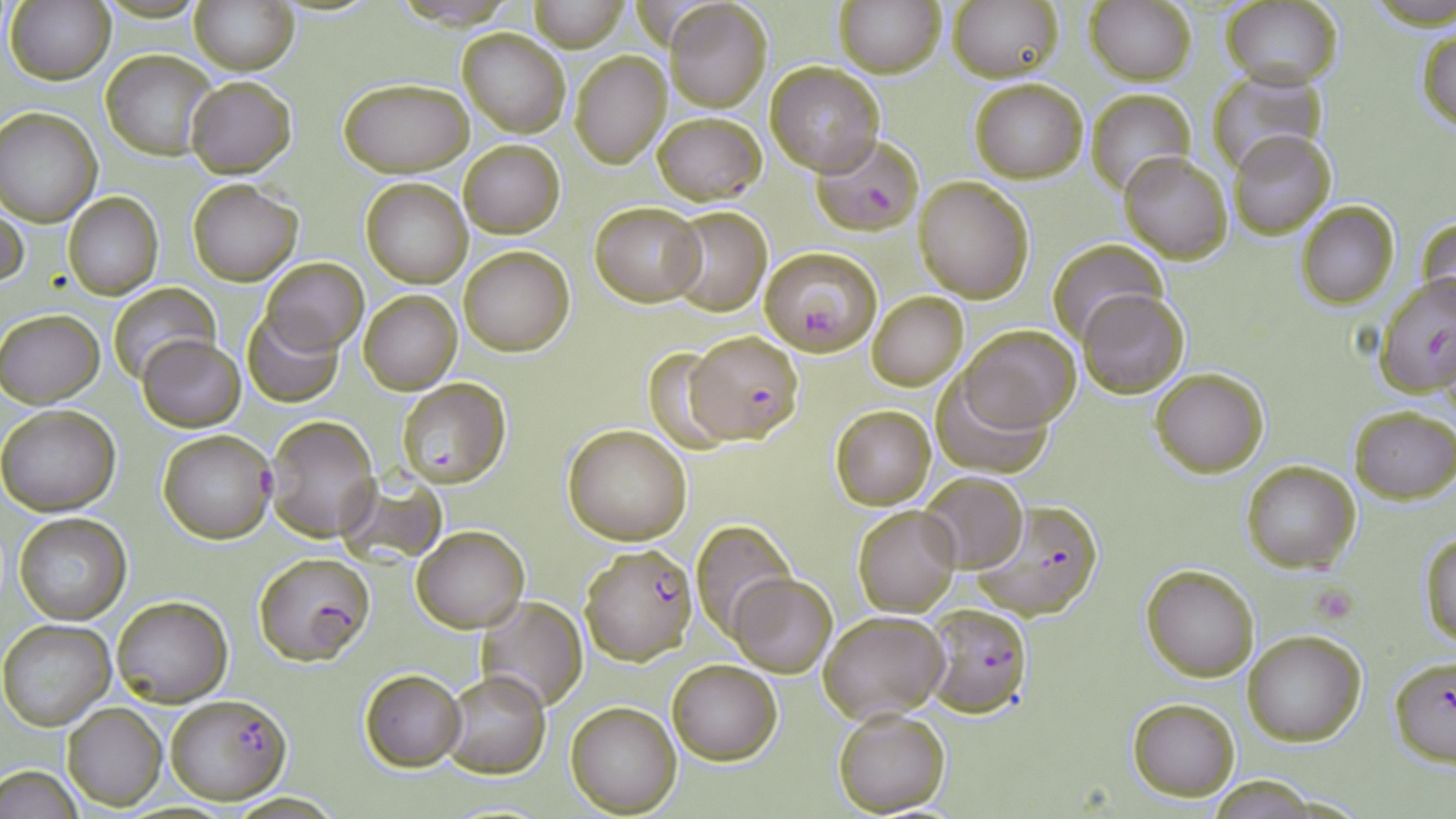

{
  "slide_level_diagnosis": "Plasmodium falciparum",
  "image_size": "1456×819 pixels",
  "magnification": "1000x",
  "preparation": "thin blood film",
  "modality": "optical microscopy",
  "stain": "May-Grünwald-Giemsa",
  "uninfected_red_blood_cell_locations_subset": "approximate bounding boxes as named x1/y1/x2/y2 corners in pixels: (x1=189, y1=0, x2=301, y2=74), (x1=529, y1=0, x2=628, y2=51), (x1=834, y1=0, x2=945, y2=77), (x1=664, y1=1, x2=772, y2=112), (x1=6, y1=2, x2=114, y2=84), (x1=948, y1=2, x2=1064, y2=81), (x1=1085, y1=2, x2=1195, y2=85), (x1=1221, y1=2, x2=1343, y2=89), (x1=1416, y1=28, x2=1456, y2=134), (x1=459, y1=29, x2=570, y2=137), (x1=100, y1=49, x2=215, y2=159), (x1=570, y1=49, x2=672, y2=168), (x1=766, y1=62, x2=886, y2=177), (x1=1206, y1=69, x2=1326, y2=177), (x1=185, y1=76, x2=296, y2=177), (x1=968, y1=76, x2=1088, y2=184), (x1=337, y1=77, x2=474, y2=176), (x1=1085, y1=89, x2=1194, y2=197), (x1=0, y1=106, x2=102, y2=225), (x1=652, y1=111, x2=766, y2=203), (x1=1227, y1=130, x2=1337, y2=239), (x1=461, y1=139, x2=564, y2=237), (x1=1118, y1=150, x2=1232, y2=262), (x1=361, y1=177, x2=472, y2=288), (x1=912, y1=177, x2=1034, y2=302), (x1=187, y1=178, x2=302, y2=286), (x1=63, y1=193, x2=163, y2=299), (x1=0, y1=196, x2=30, y2=292), (x1=590, y1=201, x2=704, y2=306), (x1=1297, y1=202, x2=1399, y2=309), (x1=664, y1=207, x2=773, y2=315), (x1=1416, y1=216, x2=1456, y2=320), (x1=1046, y1=237, x2=1167, y2=347), (x1=459, y1=245, x2=574, y2=356), (x1=261, y1=257, x2=368, y2=353), (x1=108, y1=284, x2=219, y2=384), (x1=1077, y1=288, x2=1189, y2=399), (x1=358, y1=289, x2=462, y2=395), (x1=867, y1=292, x2=968, y2=391), (x1=1, y1=309, x2=105, y2=408), (x1=243, y1=309, x2=344, y2=407), (x1=959, y1=325, x2=1081, y2=431), (x1=137, y1=334, x2=244, y2=431), (x1=643, y1=348, x2=737, y2=453), (x1=1150, y1=366, x2=1269, y2=477), (x1=932, y1=371, x2=1051, y2=478), (x1=0, y1=403, x2=121, y2=516), (x1=830, y1=404, x2=936, y2=509), (x1=1349, y1=405, x2=1455, y2=504), (x1=264, y1=415, x2=381, y2=542), (x1=563, y1=423, x2=693, y2=546), (x1=157, y1=428, x2=276, y2=545), (x1=1241, y1=461, x2=1359, y2=573), (x1=336, y1=469, x2=446, y2=568), (x1=919, y1=473, x2=1028, y2=574), (x1=852, y1=503, x2=962, y2=617), (x1=13, y1=512, x2=130, y2=625), (x1=692, y1=520, x2=796, y2=637), (x1=413, y1=526, x2=526, y2=632), (x1=1421, y1=530, x2=1456, y2=648), (x1=1141, y1=565, x2=1258, y2=680), (x1=729, y1=574, x2=837, y2=675), (x1=113, y1=596, x2=232, y2=707), (x1=479, y1=596, x2=587, y2=712), (x1=818, y1=610, x2=948, y2=721), (x1=1, y1=618, x2=118, y2=731), (x1=1243, y1=630, x2=1367, y2=745), (x1=666, y1=658, x2=783, y2=765), (x1=359, y1=668, x2=467, y2=771), (x1=440, y1=671, x2=550, y2=777), (x1=1127, y1=698, x2=1240, y2=801), (x1=566, y1=701, x2=681, y2=816), (x1=63, y1=703, x2=166, y2=811), (x1=832, y1=708, x2=950, y2=816), (x1=1, y1=764, x2=89, y2=818)",
  "plasmodium_falciparum_infected_red_blood_cell_locations_subset": "approximate bounding boxes as named x1/y1/x2/y2 corners in pixels: (x1=811, y1=131, x2=924, y2=234), (x1=759, y1=246, x2=883, y2=354), (x1=1374, y1=276, x2=1456, y2=399), (x1=397, y1=378, x2=510, y2=487), (x1=970, y1=501, x2=1104, y2=621), (x1=579, y1=544, x2=697, y2=665), (x1=253, y1=552, x2=376, y2=665), (x1=922, y1=602, x2=1032, y2=718), (x1=1389, y1=658, x2=1456, y2=764), (x1=165, y1=693, x2=291, y2=805)",
  "field_of_view": "single",
  "platelet_locations": "approximate bounding boxes as named x1/y1/x2/y2 corners in pixels: (x1=1311, y1=583, x2=1359, y2=625)"
}